Classify this cell by malaria status.
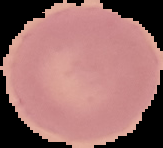

It is uninfected.

Segmented cell region on a black background. Image is 163×148 pixels. From a thin blood smear.